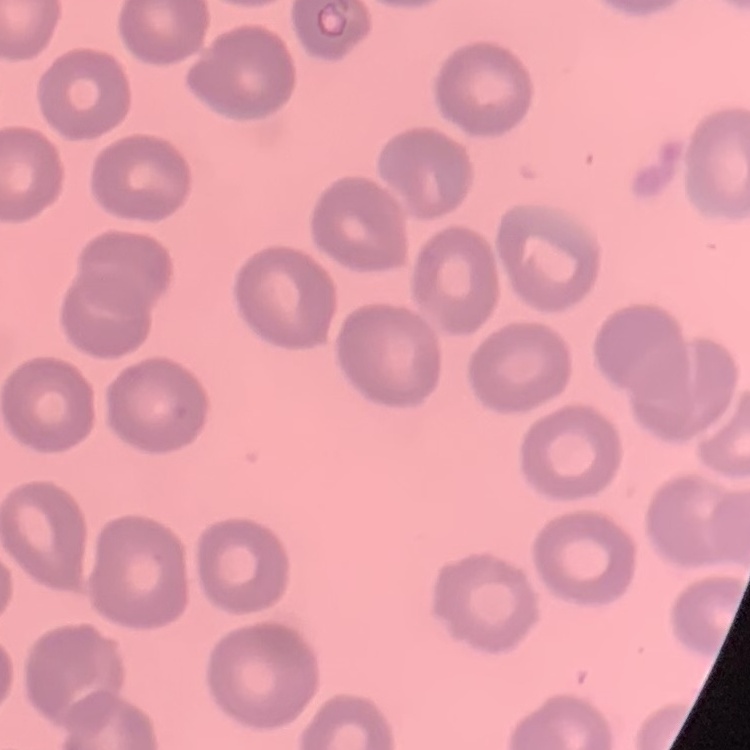 The red blood cells show no rouleaux formation. One tile cut from a larger photomicrograph. Thin peripheral smear. Stained with either Field's or Giemsa.